Classify this cell by malaria status.
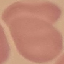
It is uninfected.

Summary:
  - Stain: Giemsa
  - Capture: smartphone camera at the microscope eyepiece
  - Image type: cell patch, automatically extracted from a larger field of view and resized to 64 × 64 pixels
  - Preparation: thin blood smear